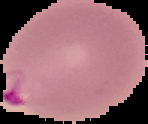

preparation: thin blood film
malaria_status: parasitized
image_size: 148×124 pixels
image_type: segmented cell region on a black background